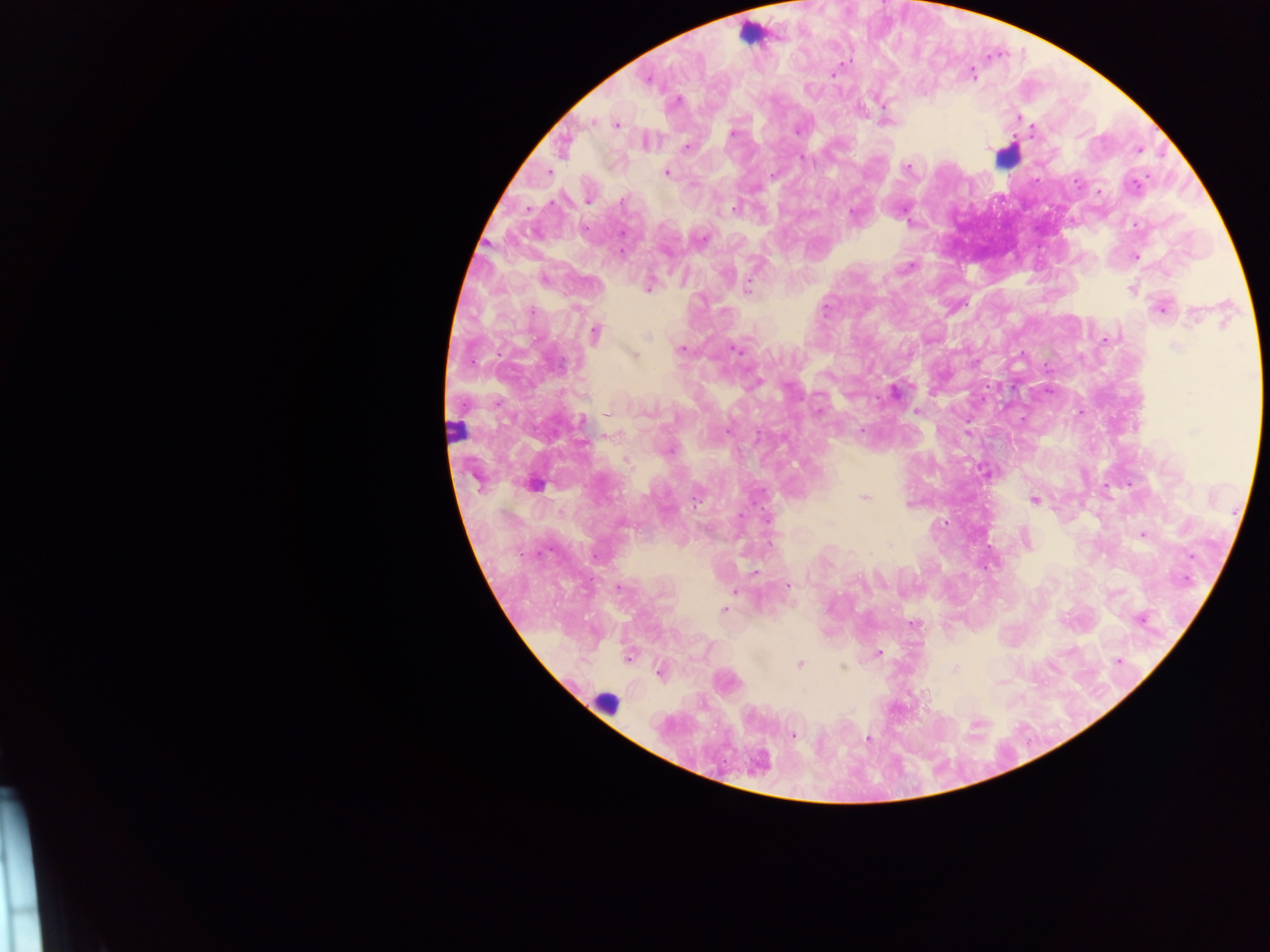

Approximate centers as [x, y] in pixels.
Summary:
  - Malaria parasite locations: [833, 73], [971, 74], [648, 80], [676, 101], [885, 121], [616, 124], [1031, 130], [732, 132], [645, 141], [686, 147], [1138, 150], [801, 156], [907, 167], [548, 172], [666, 172], [774, 174], [1099, 193], [588, 200], [735, 208], [854, 214], [1135, 256], [909, 267], [648, 286], [746, 287], [1131, 289], [1161, 307], [594, 333], [1107, 339], [681, 349], [735, 349], [634, 354], [894, 391], [1080, 411], [916, 412], [609, 414], [582, 421], [862, 430], [986, 470], [534, 484], [864, 496], [1034, 500], [766, 519], [1143, 534], [1025, 539], [754, 572], [787, 584], [618, 589], [734, 589], [724, 609], [1141, 619], [914, 624], [878, 653], [629, 656], [1118, 661], [799, 664], [843, 669], [954, 669], [660, 672], [792, 735], [868, 739], [757, 764]
  - Leukocyte locations: [751, 33], [1008, 154], [455, 431], [605, 703]
  - Capture: mobile-phone photograph through a microscope
  - Country: Ghana
  - Field of view: single
  - Preparation: thick blood film
  - Image size: 1270×952 pixels